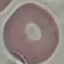
malaria status = uninfected
image type = automatically extracted cell patch, resized to 64 × 64 pixels
preparation = thin blood smear
capture = smartphone camera at the microscope eyepiece
stain = Giemsa